Outline each Plasmodium falciparum-infected red blood cell.
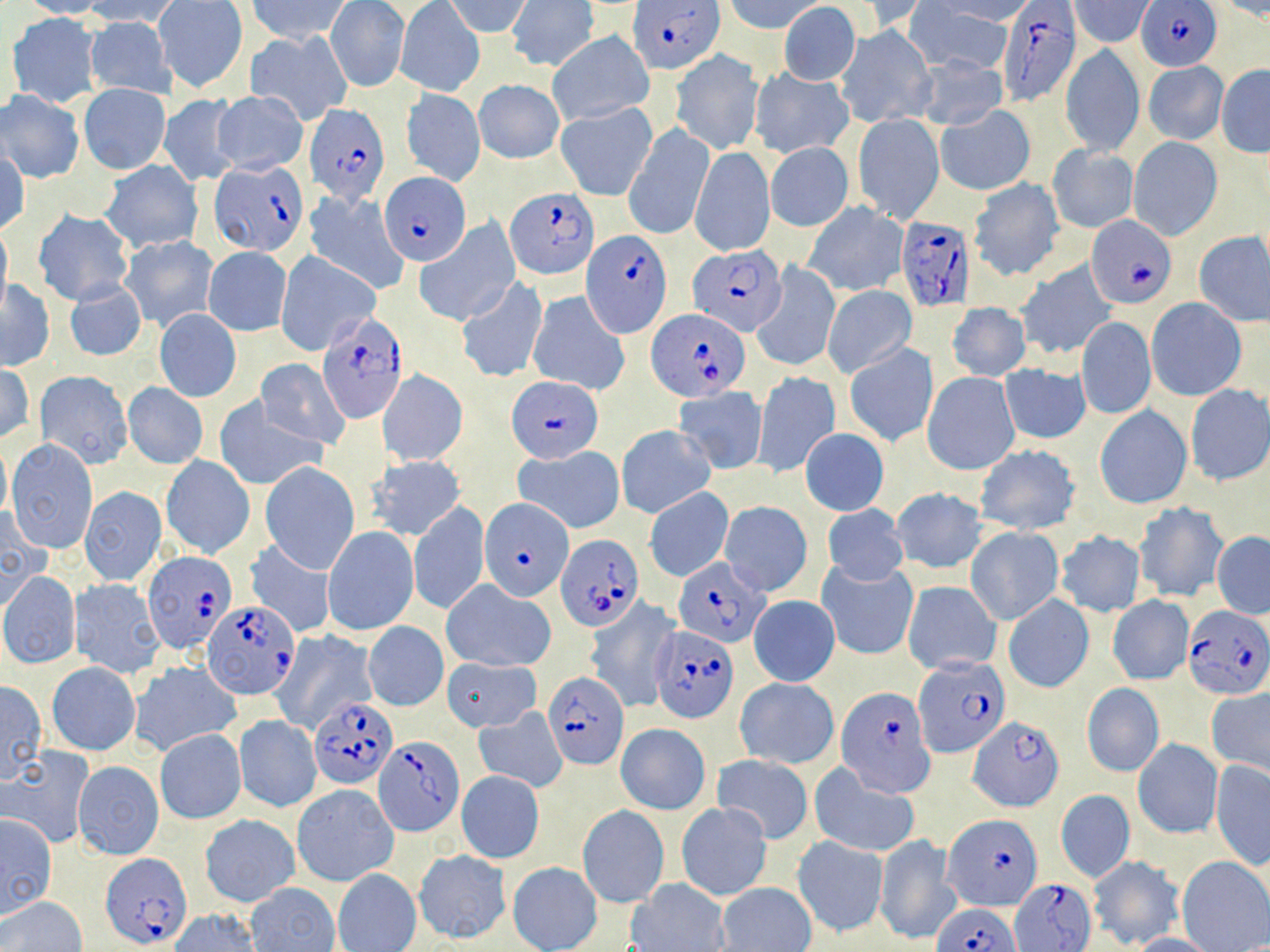

Approximate bounding boxes as (x1,y1)-(x2,y2) corner pairs in pixels.
Plasmodium falciparum-infected red blood cells (subset): (631,0)-(722,73), (1138,1)-(1222,71), (995,2)-(1081,109), (304,103)-(391,207), (209,161)-(308,258), (379,171)-(470,265), (507,188)-(598,280), (895,214)-(976,312), (1086,215)-(1176,307), (581,230)-(670,336), (685,246)-(783,337), (650,311)-(747,399), (318,312)-(411,425), (507,376)-(603,464), (480,499)-(573,601), (556,534)-(643,632), (143,553)-(239,657), (675,556)-(768,647), (203,600)-(299,699), (1180,604)-(1269,702), (651,625)-(739,723), (914,656)-(1009,759), (543,672)-(630,769), (837,687)-(935,797), (308,697)-(399,789), (969,716)-(1065,810), (943,816)-(1040,913), (100,853)-(189,950), (1011,878)-(1094,950), (931,902)-(1023,952).

Uninfected red blood cell locations (subset): (15,0)-(109,19), (82,0)-(188,27), (249,0)-(352,43), (445,0)-(532,39), (508,0)-(597,71), (724,0)-(824,34), (931,0)-(1030,24), (1071,0)-(1155,46), (325,1)-(409,92), (839,1)-(931,37), (154,2)-(247,92), (1210,2)-(1270,22), (396,3)-(482,97), (778,3)-(861,85), (910,3)-(1013,75), (6,13)-(103,107), (88,17)-(175,98), (836,24)-(936,127), (246,30)-(352,125), (548,32)-(653,124), (1060,44)-(1145,157), (671,50)-(762,154), (676,54)-(768,257), (916,54)-(1008,132), (1143,60)-(1228,145), (1216,65)-(1269,158), (751,68)-(853,159), (474,79)-(565,164), (79,84)-(171,174), (401,88)-(486,186), (0,89)-(85,184), (212,90)-(308,174), (159,94)-(241,186), (556,101)-(657,201), (936,105)-(1035,196), (852,113)-(944,223), (623,123)-(714,242), (1128,138)-(1221,239), (766,142)-(854,231), (690,145)-(775,256), (1048,145)-(1138,232), (0,149)-(29,237), (100,162)-(202,253), (968,178)-(1065,281), (303,192)-(409,295), (803,202)-(907,297), (34,209)-(135,306), (0,220)-(12,312), (414,221)-(518,325), (1193,232)-(1270,326), (120,235)-(217,332), (203,246)-(292,335), (275,253)-(378,355), (1014,259)-(1118,363), (753,264)-(839,372), (65,279)-(147,362), (455,279)-(549,382), (1,280)-(55,370), (823,286)-(917,377), (529,291)-(629,395), (1146,298)-(1246,400), (947,302)-(1031,382), (154,308)-(241,402), (1077,317)-(1156,420), (844,342)-(938,447), (255,358)-(349,449), (997,363)-(1092,447), (0,364)-(35,442), (752,370)-(839,477), (36,371)-(133,469), (376,371)-(470,465), (922,371)-(1020,476), (123,383)-(208,469), (1183,383)-(1269,487), (674,386)-(769,475), (216,399)-(324,490), (1094,405)-(1192,510), (617,425)-(716,519), (801,428)-(889,515), (7,439)-(97,553), (0,440)-(12,519), (973,445)-(1082,535), (513,446)-(625,533), (161,454)-(255,559), (366,455)-(466,541), (260,463)-(359,572), (79,486)-(166,586), (645,487)-(734,583), (890,487)-(987,575), (409,500)-(489,615), (720,500)-(811,595), (1133,500)-(1228,604), (823,503)-(907,586), (0,508)-(48,610), (323,526)-(418,637), (965,527)-(1064,624), (1054,530)-(1146,617), (1211,531)-(1270,618), (244,539)-(336,638), (818,560)-(918,661), (1,572)-(80,669), (69,578)-(167,679), (443,580)-(556,672), (902,580)-(1002,675), (1003,593)-(1093,694), (748,595)-(840,686), (1106,595)-(1194,685), (363,622)-(448,711), (269,630)-(376,734), (443,657)-(541,731), (129,660)-(241,756), (46,661)-(141,756), (735,677)-(840,768), (0,681)-(48,784), (1082,683)-(1164,777), (1205,687)-(1269,777), (474,707)-(568,792), (233,715)-(321,813), (616,724)-(711,815), (155,729)-(246,824), (1134,739)-(1222,838), (0,748)-(94,847), (711,754)-(813,843), (71,760)-(164,860), (1210,760)-(1270,869), (810,766)-(920,858), (455,770)-(545,864), (292,784)-(398,887), (1056,789)-(1134,884), (675,802)-(773,901), (577,805)-(669,907), (0,814)-(58,920), (199,815)-(301,906), (793,835)-(887,936), (875,836)-(960,943), (413,849)-(511,942), (1088,856)-(1184,949), (1178,857)-(1270,950), (507,862)-(603,951), (333,868)-(422,952), (625,879)-(730,952), (716,882)-(815,952), (245,883)-(339,952), (2,896)-(87,952), (169,909)-(263,952), (1126,931)-(1222,952). Slide-level diagnosis: Plasmodium falciparum. Thin blood film. Image is 1270×952 pixels. May-Grünwald-Giemsa stain. 1000x magnification. One field of a larger specimen. Optical microscopy.